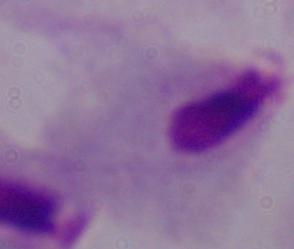
Photomicrograph. A trichomonad is seen. Captured at 1000x magnification.